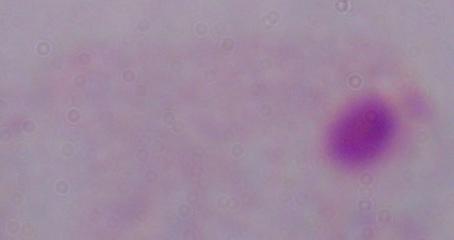

Captured at 1000x magnification. A trichomonad is shown. Micrograph.